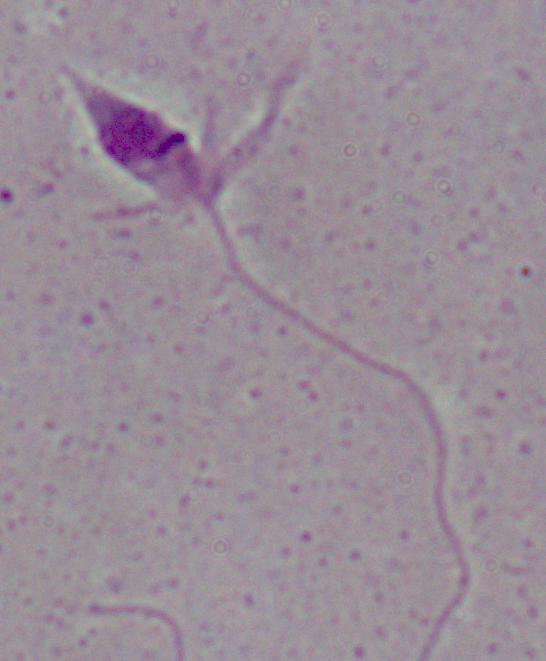

1000x magnification. A Leishmania parasite is shown. Micrograph.